Assess this cell for malaria.
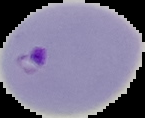

It is parasitized.

image size = 145×118 pixels
image type = segmented cell region with the area outside set to black
preparation = thin blood film